Outline each blood parasite and name the species.
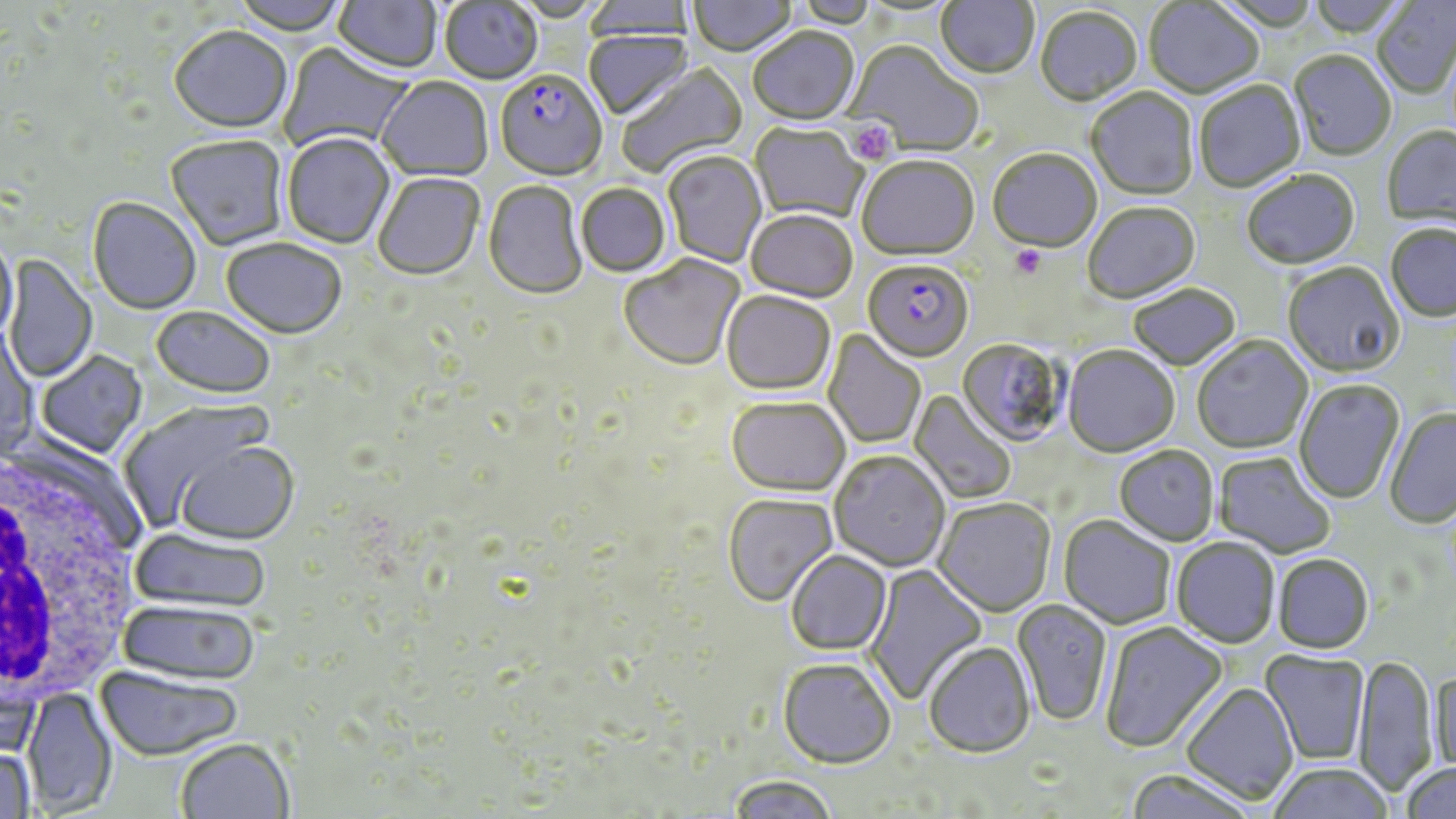
Approximate bounding boxes as named x1/y1/x2/y2 corners in pixels.
Plasmodium falciparum-infected red blood cells: (x1=495, y1=73, x2=607, y2=183), (x1=863, y1=260, x2=973, y2=362).
No Plasmodium ovale, Plasmodium malariae, Plasmodium vivax, Babesia divergens, or Trypanosoma brucei observed.

Summary:
  - Platelet locations: (x1=847, y1=120, x2=895, y2=165), (x1=1010, y1=246, x2=1046, y2=280)
  - White blood cell locations: (x1=0, y1=445, x2=142, y2=704)
  - Uninfected red blood cell locations: (x1=230, y1=0, x2=351, y2=37), (x1=333, y1=0, x2=442, y2=76), (x1=688, y1=0, x2=798, y2=58), (x1=934, y1=0, x2=1039, y2=81), (x1=1305, y1=0, x2=1407, y2=40), (x1=1372, y1=0, x2=1456, y2=100), (x1=582, y1=1, x2=696, y2=41), (x1=1143, y1=1, x2=1264, y2=101), (x1=440, y1=2, x2=543, y2=86), (x1=792, y1=2, x2=878, y2=29), (x1=1035, y1=9, x2=1143, y2=107), (x1=168, y1=28, x2=293, y2=135), (x1=748, y1=29, x2=860, y2=127), (x1=584, y1=30, x2=693, y2=122), (x1=846, y1=42, x2=983, y2=156), (x1=278, y1=43, x2=413, y2=152), (x1=1288, y1=52, x2=1396, y2=163), (x1=617, y1=63, x2=749, y2=178), (x1=377, y1=78, x2=493, y2=183), (x1=1194, y1=81, x2=1306, y2=194), (x1=1086, y1=89, x2=1199, y2=201), (x1=748, y1=124, x2=868, y2=224), (x1=1381, y1=126, x2=1456, y2=232), (x1=282, y1=134, x2=396, y2=250), (x1=166, y1=136, x2=288, y2=252), (x1=987, y1=150, x2=1102, y2=255), (x1=663, y1=151, x2=767, y2=269), (x1=856, y1=157, x2=979, y2=262), (x1=1242, y1=171, x2=1360, y2=271), (x1=373, y1=174, x2=485, y2=282), (x1=483, y1=181, x2=587, y2=302), (x1=576, y1=184, x2=671, y2=278), (x1=88, y1=198, x2=201, y2=315), (x1=1083, y1=203, x2=1201, y2=305), (x1=746, y1=211, x2=858, y2=303), (x1=1384, y1=225, x2=1456, y2=324), (x1=0, y1=236, x2=18, y2=343), (x1=221, y1=239, x2=348, y2=341), (x1=4, y1=255, x2=97, y2=384), (x1=619, y1=255, x2=745, y2=372), (x1=1282, y1=262, x2=1405, y2=380), (x1=1128, y1=284, x2=1240, y2=371), (x1=721, y1=290, x2=836, y2=396), (x1=150, y1=307, x2=275, y2=401), (x1=0, y1=325, x2=40, y2=458), (x1=823, y1=330, x2=927, y2=449), (x1=1192, y1=336, x2=1313, y2=454), (x1=957, y1=338, x2=1069, y2=447), (x1=1063, y1=346, x2=1179, y2=457), (x1=36, y1=351, x2=148, y2=459), (x1=1293, y1=379, x2=1405, y2=505), (x1=910, y1=390, x2=1017, y2=505), (x1=727, y1=396, x2=850, y2=495), (x1=118, y1=399, x2=278, y2=531), (x1=1384, y1=408, x2=1456, y2=529), (x1=171, y1=440, x2=300, y2=545), (x1=1114, y1=445, x2=1219, y2=546), (x1=829, y1=451, x2=950, y2=571), (x1=1212, y1=451, x2=1336, y2=560), (x1=723, y1=493, x2=838, y2=607), (x1=933, y1=498, x2=1056, y2=617), (x1=1059, y1=516, x2=1176, y2=629), (x1=128, y1=527, x2=272, y2=613), (x1=1172, y1=538, x2=1280, y2=648), (x1=785, y1=550, x2=892, y2=655), (x1=1272, y1=553, x2=1374, y2=653), (x1=864, y1=563, x2=987, y2=705), (x1=116, y1=600, x2=260, y2=685), (x1=1012, y1=600, x2=1113, y2=726), (x1=1099, y1=622, x2=1228, y2=753), (x1=923, y1=642, x2=1035, y2=757), (x1=1261, y1=651, x2=1370, y2=765), (x1=1353, y1=655, x2=1439, y2=797), (x1=777, y1=658, x2=896, y2=768), (x1=95, y1=666, x2=243, y2=760), (x1=0, y1=667, x2=41, y2=759), (x1=1431, y1=669, x2=1456, y2=775), (x1=1182, y1=682, x2=1299, y2=804), (x1=22, y1=687, x2=117, y2=816), (x1=174, y1=737, x2=294, y2=819), (x1=0, y1=744, x2=35, y2=819), (x1=1401, y1=761, x2=1456, y2=818), (x1=1267, y1=762, x2=1394, y2=819), (x1=1123, y1=768, x2=1259, y2=819), (x1=727, y1=775, x2=838, y2=819)
  - Slide-level diagnosis: Plasmodium falciparum
  - Modality: light microscopy
  - Field of view: one of a larger specimen
  - Preparation: thin blood smear
  - Image size: 1456×819 pixels
  - Magnification: 1000x
  - Stain: May-Grünwald-Giemsa